Identify the parasite.
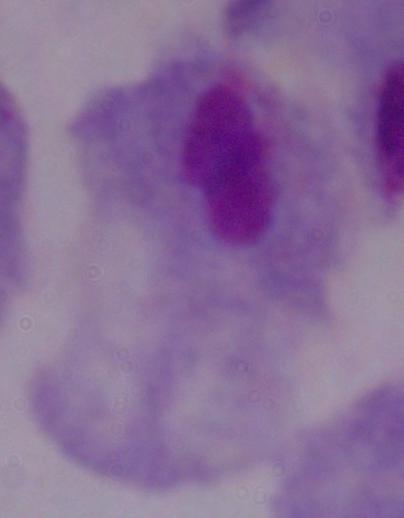

This is a trichomonad.

1000x magnification. Micrograph.